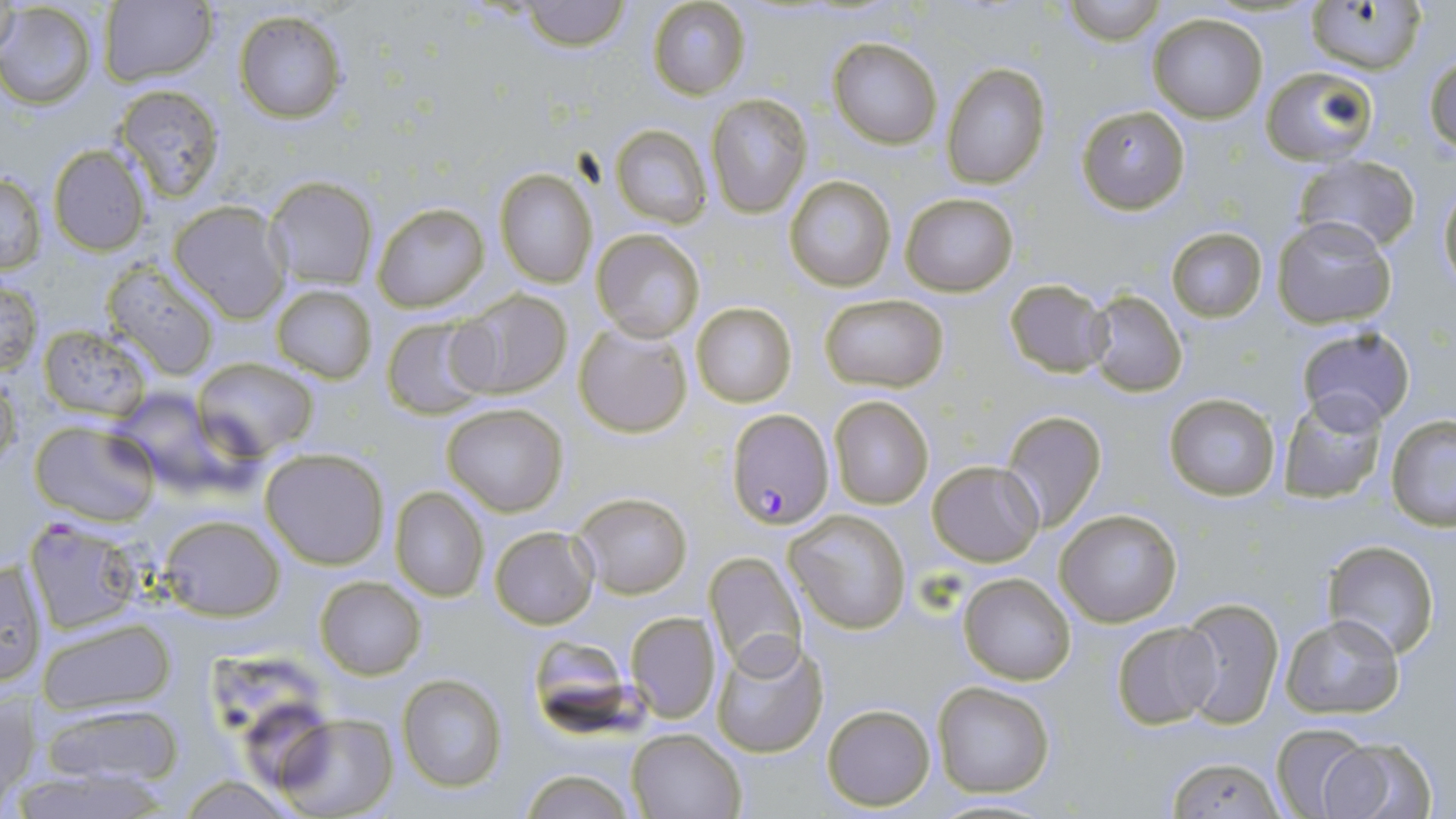
Summary:
  - Coordinate format: approximate bounding boxes as (x1,y1)-(x2,y2) corner pairs in pixels
  - Uninfected red blood cell locations: (1,0)-(22,60), (1065,0)-(1164,45), (518,1)-(633,51), (647,1)-(750,101), (1308,1)-(1428,73), (0,2)-(98,109), (99,2)-(217,85), (234,11)-(347,124), (1148,13)-(1267,123), (827,35)-(942,149), (1425,53)-(1456,159), (943,64)-(1049,188), (1263,66)-(1379,165), (114,84)-(225,201), (706,92)-(811,218), (1077,104)-(1189,216), (610,125)-(711,228), (46,143)-(152,256), (1293,154)-(1421,255), (494,167)-(597,289), (1,171)-(47,274), (784,174)-(896,293), (264,176)-(378,289), (1438,181)-(1456,295), (900,192)-(1018,295), (168,201)-(291,321), (371,202)-(489,313), (1270,216)-(1399,330), (1166,227)-(1268,321), (591,229)-(703,342), (101,263)-(221,380), (0,277)-(44,376), (1005,278)-(1112,379), (270,284)-(377,383), (450,288)-(573,401), (1087,289)-(1188,396), (818,293)-(950,392), (692,303)-(797,408), (382,316)-(490,420), (573,321)-(693,440), (1294,324)-(1416,429), (38,325)-(155,420), (193,356)-(320,457), (0,370)-(21,470), (1277,392)-(1389,504), (1162,393)-(1281,500), (828,394)-(934,510), (440,401)-(568,515), (1000,409)-(1108,533), (1386,415)-(1456,529), (30,421)-(160,526), (260,447)-(389,570), (928,461)-(1043,567), (389,485)-(489,601), (570,491)-(692,599), (1055,506)-(1184,628), (788,510)-(912,635), (158,514)-(285,619), (24,518)-(145,635), (490,526)-(598,628), (1324,540)-(1441,661), (702,551)-(807,675), (1,559)-(48,689), (956,572)-(1077,685), (314,575)-(426,680), (1175,596)-(1285,729), (626,611)-(720,722), (1280,613)-(1408,719), (38,619)-(175,715), (1110,620)-(1222,731), (710,632)-(831,758), (397,675)-(508,792), (932,681)-(1055,800), (1,690)-(37,805), (34,700)-(189,792), (821,704)-(935,811), (272,714)-(399,819), (1272,723)-(1374,817), (626,727)-(746,818), (1314,736)-(1439,819), (1162,755)-(1284,818), (12,766)-(172,819), (517,767)-(637,819), (177,775)-(298,816)
  - Plasmodium falciparum-infected red blood cell locations: (728,411)-(834,531)
  - Slide-level diagnosis: Plasmodium falciparum
  - Field of view: one of a larger specimen
  - Preparation: thin blood smear
  - Stain: May-Grünwald-Giemsa
  - Image size: 1456×819 pixels
  - Magnification: 1000x
  - Modality: light microscopy